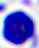
modality = micrograph
identification = leukocyte
magnification = 400x